Give the extent of all uninfected red blood cells.
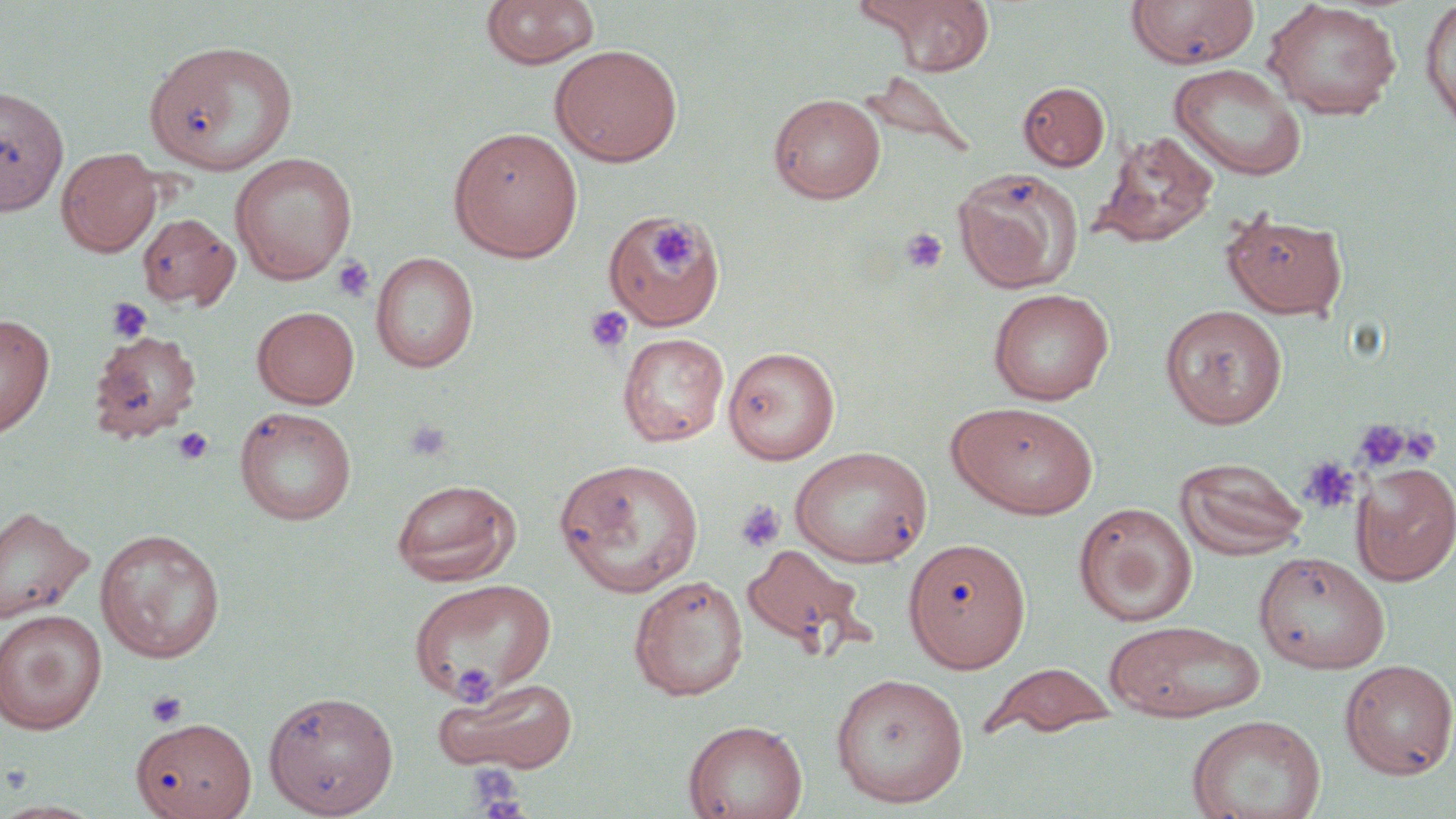

Approximate bounding boxes as (x1,y1)-(x2,y2) corner pairs in pixels.
Uninfected red blood cells: (480,0)-(600,71), (876,0)-(994,74), (1126,0)-(1260,69), (1263,1)-(1402,120), (1420,1)-(1456,134), (146,40)-(296,174), (550,44)-(683,167), (1168,62)-(1307,181), (861,71)-(978,159), (1018,81)-(1109,171), (0,85)-(69,216), (769,93)-(886,203), (447,125)-(583,261), (1094,131)-(1218,248), (56,148)-(162,256), (230,152)-(357,284), (953,166)-(1083,292), (1220,208)-(1348,320), (602,211)-(726,328), (137,213)-(239,310), (370,252)-(479,373), (988,288)-(1114,405), (1160,304)-(1288,429), (252,306)-(359,409), (0,313)-(54,437), (88,330)-(202,443), (617,332)-(730,447), (722,346)-(840,464), (947,402)-(1099,519), (234,406)-(357,525), (789,445)-(932,568), (1175,456)-(1309,560), (1295,457)-(1358,513), (554,459)-(705,598), (1351,461)-(1456,585), (390,478)-(520,586), (1073,502)-(1197,627), (0,506)-(94,624), (94,529)-(226,663), (903,537)-(1031,672), (740,543)-(870,657), (1253,551)-(1390,672), (628,574)-(748,702), (408,578)-(557,703), (0,609)-(107,735), (1104,620)-(1266,723), (1339,659)-(1456,779), (981,662)-(1118,741), (830,672)-(969,808), (436,677)-(579,773), (262,689)-(399,817), (1186,714)-(1326,819), (131,718)-(257,818), (683,719)-(808,819), (0,800)-(103,817).

Platelet locations: (649,221)-(697,270), (900,227)-(948,274), (332,255)-(376,303), (106,297)-(152,343), (584,305)-(634,354), (1353,418)-(1411,472), (405,419)-(453,461), (172,426)-(214,465), (1408,431)-(1441,469), (1299,455)-(1359,515), (734,500)-(786,553), (146,689)-(188,729), (465,765)-(525,813). Slide-level diagnosis: negative for blood parasites. May-Grünwald-Giemsa-stained preparation. Image is 1456×819 pixels. Light microscopy. Captured at 1000x magnification. Thin blood smear. One field of a larger specimen.